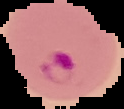

malaria status = parasitized
preparation = thin blood smear
image size = 124×109 pixels
image type = cell region segmented out of the field of view; surrounding area masked to black